Identify the cell.
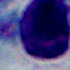

A leukocyte.

Captured at 1000x magnification. Photomicrograph.